Locate every blood parasite and identify its species.
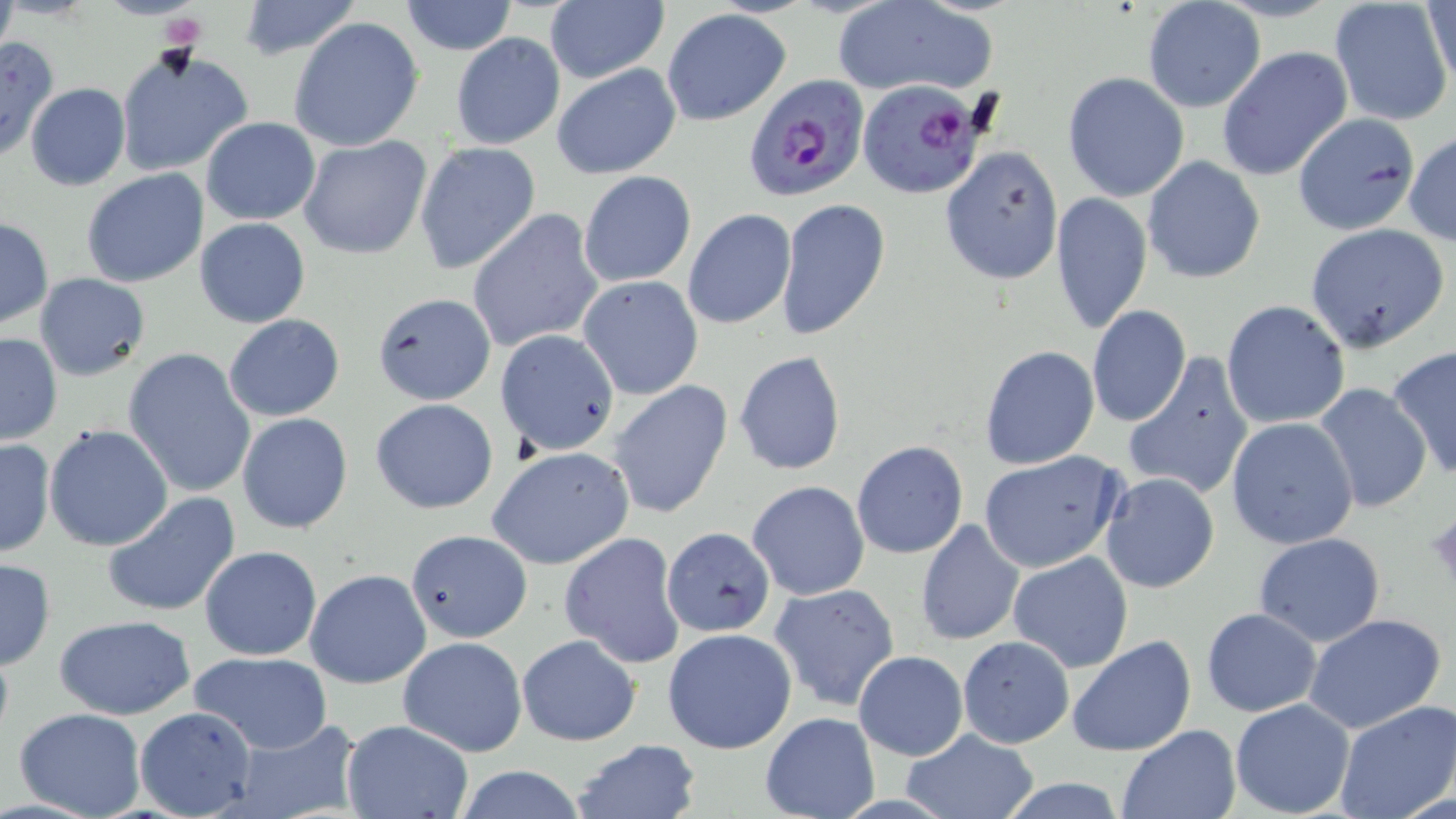

Approximate bounding boxes as named x1/y1/x2/y2 corners in pixels.
Plasmodium falciparum-infected red blood cells: (x1=744, y1=75, x2=872, y2=200), (x1=858, y1=77, x2=985, y2=200).
No Plasmodium ovale, Plasmodium malariae, Plasmodium vivax, Babesia divergens, or Trypanosoma brucei observed.

slide-level diagnosis = Plasmodium falciparum
uninfected red blood cell locations = approximate bounding boxes as named x1/y1/x2/y2 corners in pixels: (x1=232, y1=0, x2=363, y2=60), (x1=398, y1=0, x2=519, y2=55), (x1=834, y1=0, x2=996, y2=96), (x1=1423, y1=0, x2=1456, y2=91), (x1=1141, y1=1, x2=1266, y2=113), (x1=1329, y1=1, x2=1455, y2=125), (x1=544, y1=3, x2=667, y2=84), (x1=661, y1=9, x2=791, y2=126), (x1=288, y1=17, x2=425, y2=152), (x1=449, y1=32, x2=567, y2=151), (x1=0, y1=34, x2=58, y2=162), (x1=114, y1=47, x2=251, y2=178), (x1=1216, y1=47, x2=1353, y2=181), (x1=551, y1=64, x2=682, y2=180), (x1=1062, y1=73, x2=1190, y2=202), (x1=24, y1=82, x2=131, y2=191), (x1=1292, y1=112, x2=1421, y2=236), (x1=200, y1=118, x2=321, y2=224), (x1=1403, y1=132, x2=1456, y2=246), (x1=299, y1=135, x2=433, y2=260), (x1=414, y1=142, x2=541, y2=274), (x1=941, y1=146, x2=1065, y2=286), (x1=1142, y1=156, x2=1266, y2=284), (x1=80, y1=168, x2=209, y2=287), (x1=578, y1=170, x2=696, y2=287), (x1=1050, y1=192, x2=1152, y2=335), (x1=775, y1=199, x2=889, y2=343), (x1=467, y1=208, x2=605, y2=354), (x1=683, y1=208, x2=796, y2=329), (x1=0, y1=216, x2=51, y2=329), (x1=194, y1=217, x2=312, y2=329), (x1=1304, y1=223, x2=1449, y2=352), (x1=34, y1=273, x2=152, y2=382), (x1=577, y1=274, x2=704, y2=400), (x1=372, y1=291, x2=496, y2=405), (x1=1221, y1=299, x2=1350, y2=430), (x1=1087, y1=305, x2=1190, y2=427), (x1=224, y1=314, x2=344, y2=422), (x1=494, y1=329, x2=619, y2=456), (x1=0, y1=331, x2=63, y2=446), (x1=1385, y1=345, x2=1456, y2=483), (x1=122, y1=346, x2=257, y2=498), (x1=979, y1=346, x2=1100, y2=470), (x1=734, y1=351, x2=846, y2=475), (x1=1122, y1=354, x2=1256, y2=503), (x1=610, y1=381, x2=733, y2=520), (x1=1313, y1=384, x2=1431, y2=515), (x1=371, y1=398, x2=499, y2=515), (x1=237, y1=412, x2=353, y2=534), (x1=1226, y1=417, x2=1359, y2=549), (x1=43, y1=424, x2=174, y2=552), (x1=0, y1=437, x2=55, y2=559), (x1=851, y1=440, x2=969, y2=560), (x1=488, y1=447, x2=636, y2=571), (x1=977, y1=452, x2=1127, y2=574), (x1=1100, y1=474, x2=1220, y2=592), (x1=746, y1=480, x2=869, y2=600), (x1=102, y1=492, x2=241, y2=618), (x1=1427, y1=507, x2=1456, y2=596), (x1=915, y1=518, x2=1025, y2=646), (x1=661, y1=526, x2=776, y2=637), (x1=406, y1=529, x2=532, y2=644), (x1=560, y1=531, x2=686, y2=669), (x1=1252, y1=531, x2=1388, y2=645), (x1=198, y1=545, x2=323, y2=662), (x1=1008, y1=551, x2=1134, y2=673), (x1=0, y1=557, x2=55, y2=671), (x1=305, y1=567, x2=432, y2=688), (x1=769, y1=583, x2=901, y2=713), (x1=1200, y1=609, x2=1321, y2=717), (x1=1302, y1=612, x2=1448, y2=735), (x1=54, y1=614, x2=196, y2=719), (x1=662, y1=628, x2=800, y2=755), (x1=516, y1=633, x2=641, y2=746), (x1=1066, y1=634, x2=1197, y2=758), (x1=956, y1=635, x2=1075, y2=749), (x1=397, y1=636, x2=528, y2=757), (x1=853, y1=650, x2=968, y2=760), (x1=186, y1=651, x2=333, y2=754), (x1=1230, y1=698, x2=1357, y2=818), (x1=1333, y1=700, x2=1456, y2=819), (x1=136, y1=706, x2=257, y2=816), (x1=13, y1=708, x2=146, y2=819), (x1=760, y1=712, x2=880, y2=819), (x1=223, y1=719, x2=361, y2=819), (x1=340, y1=719, x2=475, y2=818), (x1=1116, y1=725, x2=1241, y2=818), (x1=901, y1=729, x2=1039, y2=818), (x1=571, y1=739, x2=701, y2=819), (x1=451, y1=764, x2=591, y2=819), (x1=994, y1=779, x2=1133, y2=816)
image size = 1456×819 pixels
stain = May-Grünwald-Giemsa
platelet locations = approximate bounding boxes as named x1/y1/x2/y2 corners in pixels: (x1=161, y1=14, x2=205, y2=52)
modality = light microscopy
magnification = 1000x
field of view = one of a larger specimen
preparation = thin blood film